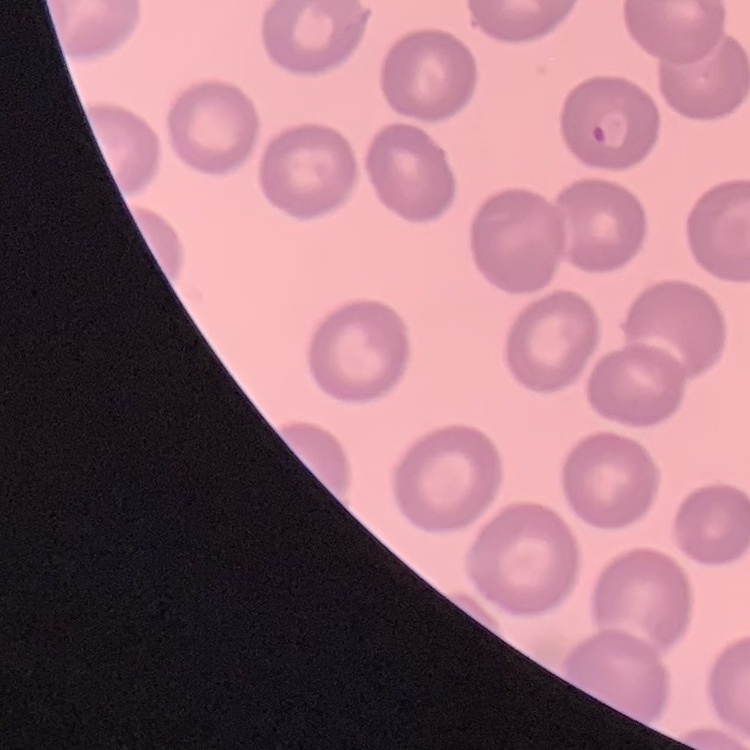
{
  "red_blood_cell_morphology": "no rouleaux formation",
  "stain": "Field's or Giemsa",
  "image_type": "square crop of a larger photomicrograph",
  "preparation": "thin blood film"
}